State the blood parasite species.
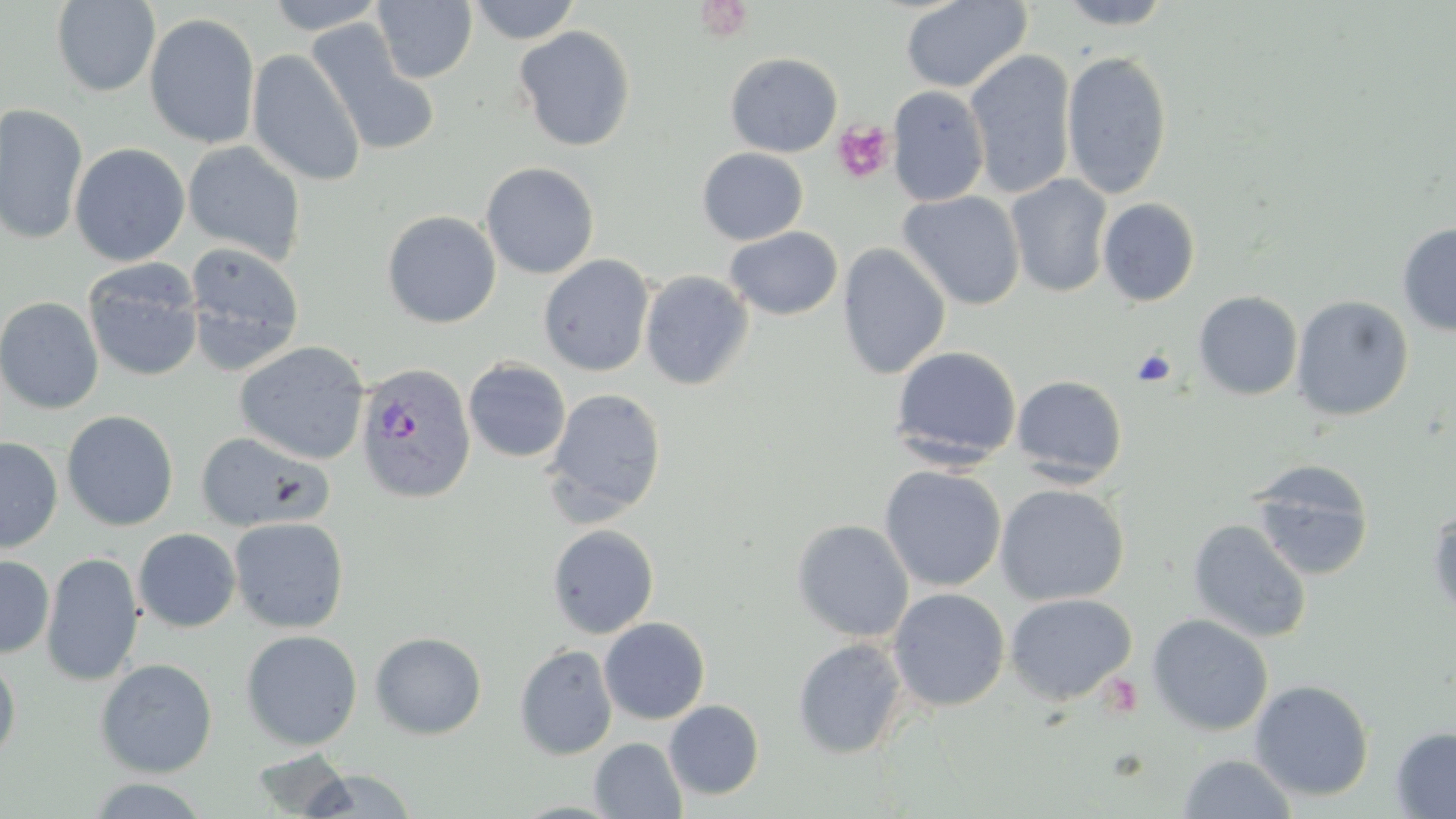
Plasmodium vivax.

platelet locations = approximate bounding boxes as [x1, y1, x2, y2] in pixels: [832, 121, 894, 184], [1131, 349, 1176, 387]
preparation = thin blood smear
stain = May-Grünwald-Giemsa
magnification = 1000x
modality = light microscopy
image size = 1456×819 pixels
field of view = single
uninfected red blood cell locations = approximate bounding boxes as [x1, y1, x2, y2] in pixels: [263, 0, 389, 34], [468, 0, 581, 45], [901, 0, 1032, 94], [1054, 0, 1177, 29], [51, 1, 160, 97], [372, 1, 477, 83], [143, 12, 261, 149], [305, 19, 441, 156], [513, 25, 636, 152], [246, 48, 366, 187], [965, 49, 1077, 199], [1061, 50, 1172, 199], [724, 52, 843, 157], [887, 84, 990, 207], [0, 103, 88, 247], [182, 141, 306, 266], [69, 142, 190, 266], [697, 147, 809, 245], [480, 162, 600, 279], [1006, 173, 1113, 298], [897, 190, 1026, 310], [1097, 197, 1201, 306], [382, 210, 501, 328], [1396, 223, 1456, 337], [724, 226, 843, 320], [184, 242, 305, 374], [837, 243, 952, 380], [537, 254, 655, 377], [83, 260, 203, 382], [639, 270, 754, 390], [1193, 290, 1303, 400], [1291, 295, 1414, 421], [0, 296, 104, 415], [234, 341, 370, 465], [890, 345, 1022, 467], [463, 358, 571, 463], [1011, 375, 1128, 484], [543, 388, 667, 525], [61, 410, 179, 531], [197, 430, 335, 532], [0, 437, 62, 553], [1248, 461, 1374, 581], [879, 465, 1006, 592], [994, 483, 1129, 606], [1427, 507, 1456, 622], [228, 517, 349, 633], [791, 518, 914, 642], [1187, 519, 1311, 643], [547, 524, 660, 639], [132, 528, 241, 632], [41, 552, 143, 687], [0, 555, 54, 658], [887, 588, 1010, 712], [1003, 592, 1138, 706], [1147, 613, 1273, 736], [599, 617, 710, 724], [240, 630, 363, 751], [370, 632, 487, 740], [792, 637, 909, 759], [514, 644, 617, 760], [0, 656, 21, 764], [95, 659, 217, 778], [1249, 679, 1375, 801], [664, 700, 764, 800], [1390, 726, 1456, 817], [589, 737, 687, 818], [249, 748, 355, 817], [1177, 753, 1298, 818], [300, 769, 419, 817], [82, 777, 214, 818]
Plasmodium vivax-infected red blood cell locations = approximate bounding boxes as [x1, y1, x2, y2] in pixels: [354, 361, 477, 504]